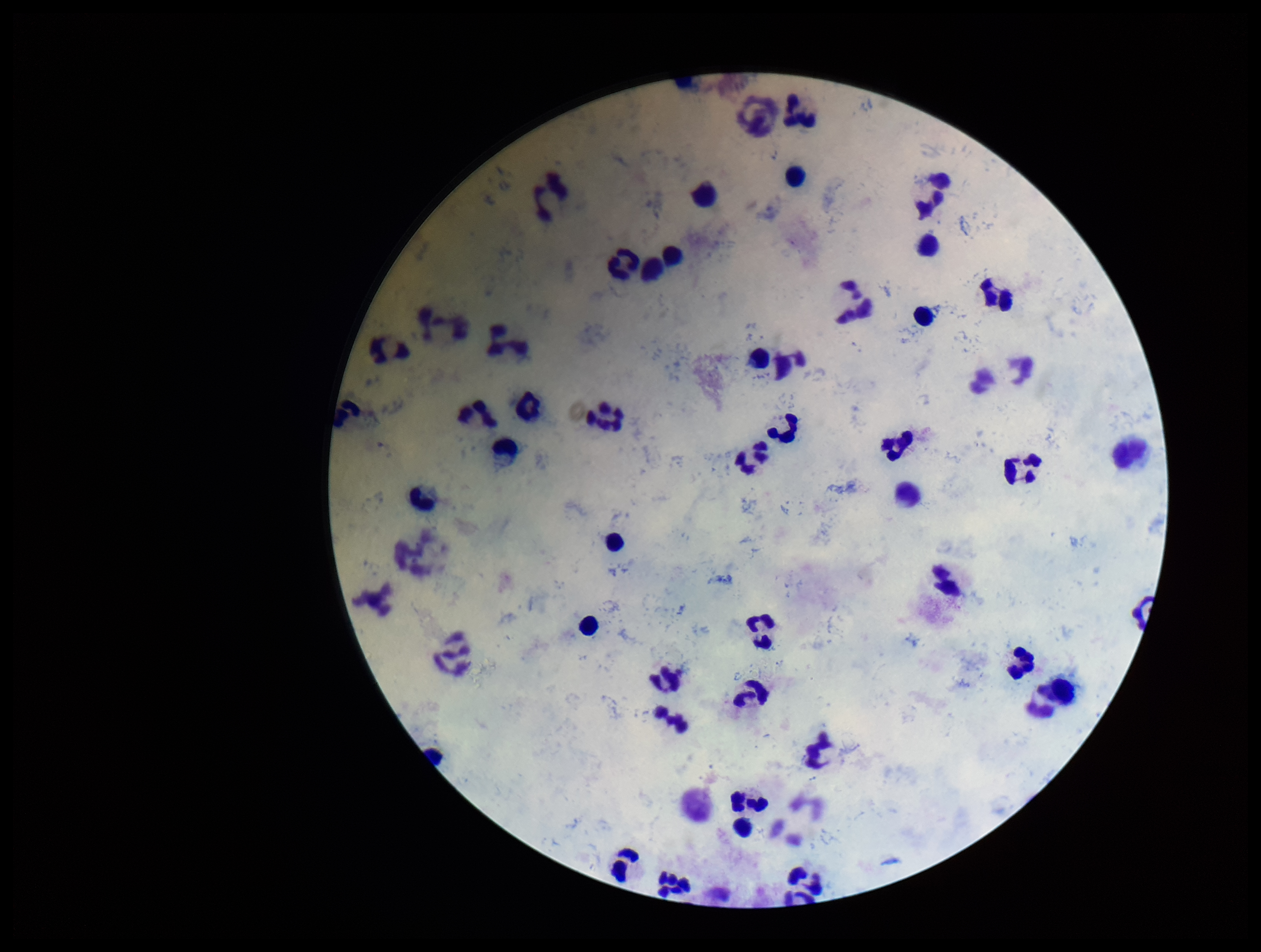

Summary:
  - Leukocyte count: 48
  - Parasite count: 0
  - Stain: Giemsa
  - Image size: 1261×952 pixels
  - Field of view: single
  - Capture: smartphone photograph through the microscope eyepiece
  - Plasmodium parasites: none identified
  - Preparation: thick
  - Patient malaria status: negative